Identify the parasite.
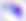

This is Toxoplasma gondii.

400x magnification. Photomicrograph.